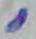
Summary:
  - Magnification: 1000x
  - Modality: micrograph
  - Identification: Toxoplasma gondii